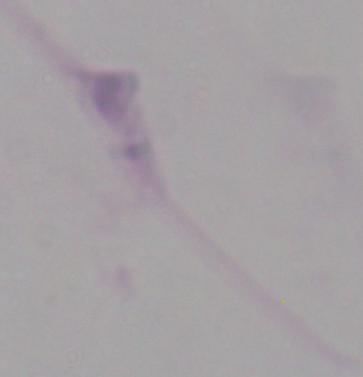

Captured at 1000x magnification. Photomicrograph. A Leishmania parasite is shown.